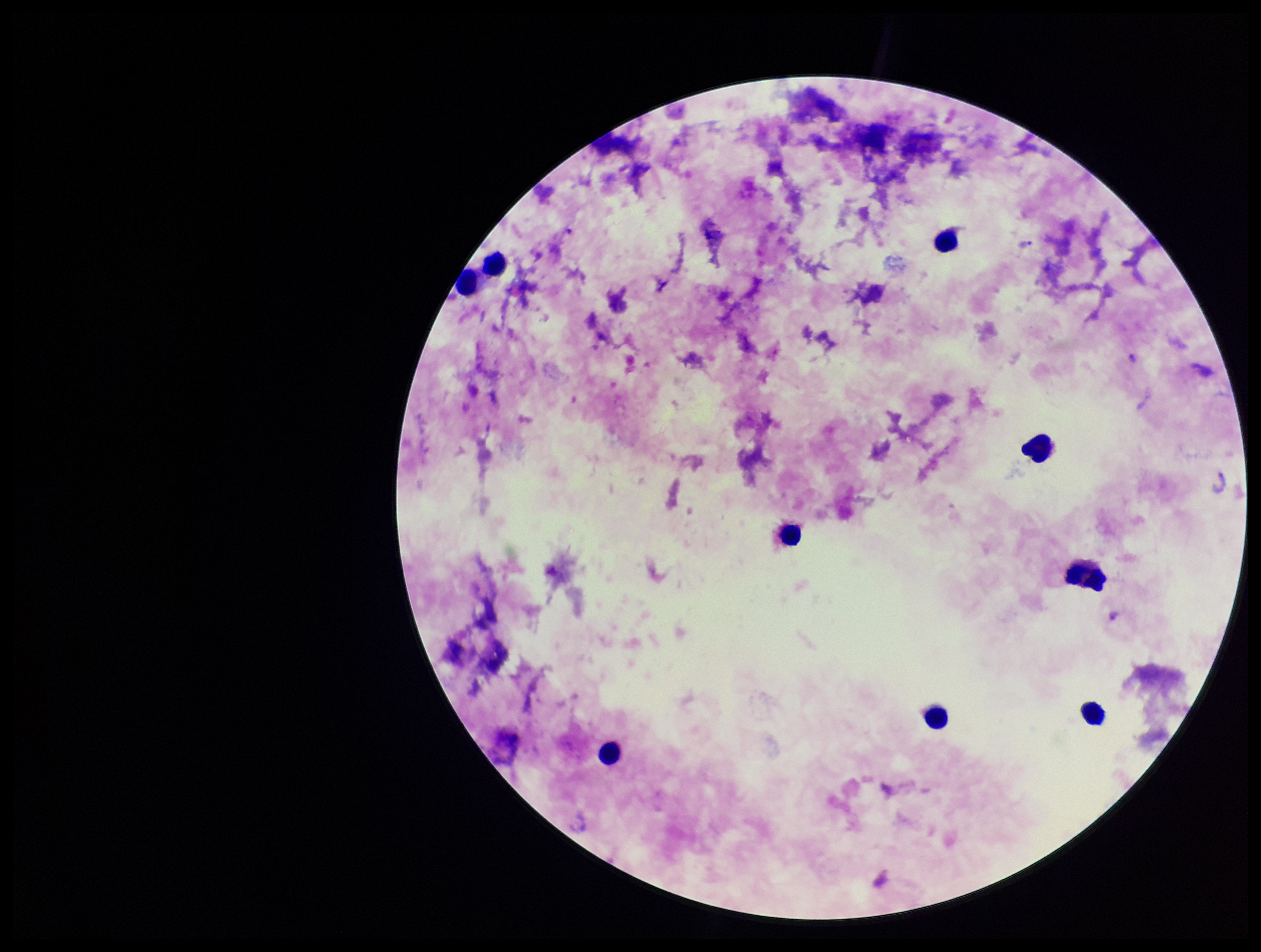

Plasmodium parasites = identified
species reported for this patient = Plasmodium falciparum
parasite count = 2
stain = Giemsa
leukocyte count = 9
preparation = thick smear
image size = 1261×952 pixels
capture = smartphone photograph through the microscope eyepiece
patient malaria status = infected
field of view = single